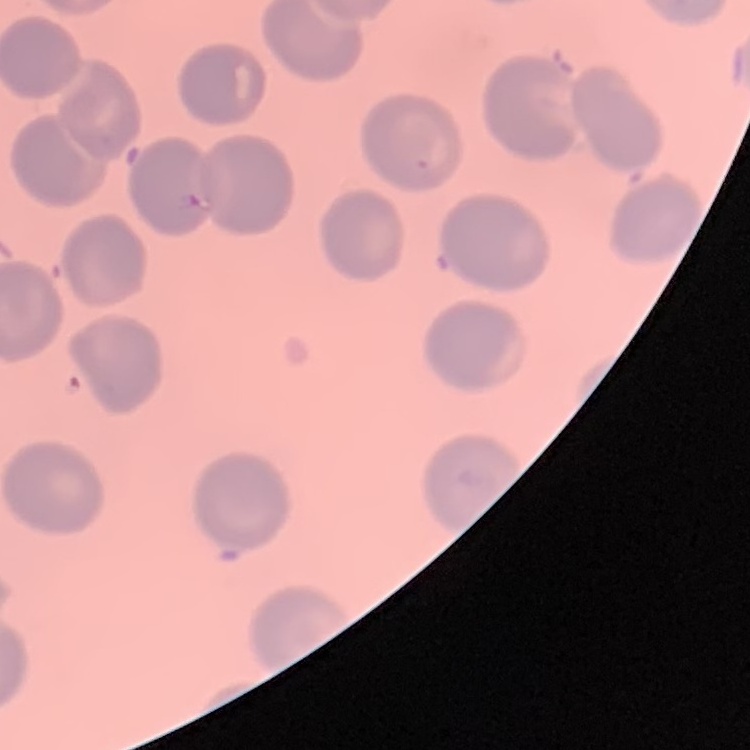 The red blood cells show no rouleaux formation. One tile cut from a larger photomicrograph. Field's or Giemsa stain. Thin blood smear.